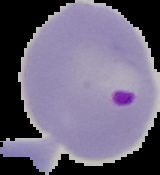 Result: malaria parasites identified. The area outside the segmented cell region is set to black. Image is 160×175 pixels. From a thin blood film.